Classify this cell by malaria status.
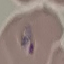
Parasitized.

capture = smartphone camera at the microscope eyepiece
stain = Giemsa
preparation = thin blood smear
image type = cell patch, automatically extracted from a larger field of view and resized to 64 × 64 pixels